Classify this cell by malaria status.
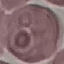

Uninfected.

{
  "preparation": "thin blood film",
  "image_type": "automatically extracted cell patch, resized to 64 × 64 pixels",
  "capture": "smartphone camera at the microscope eyepiece",
  "stain": "Giemsa"
}